Give the preparation type.
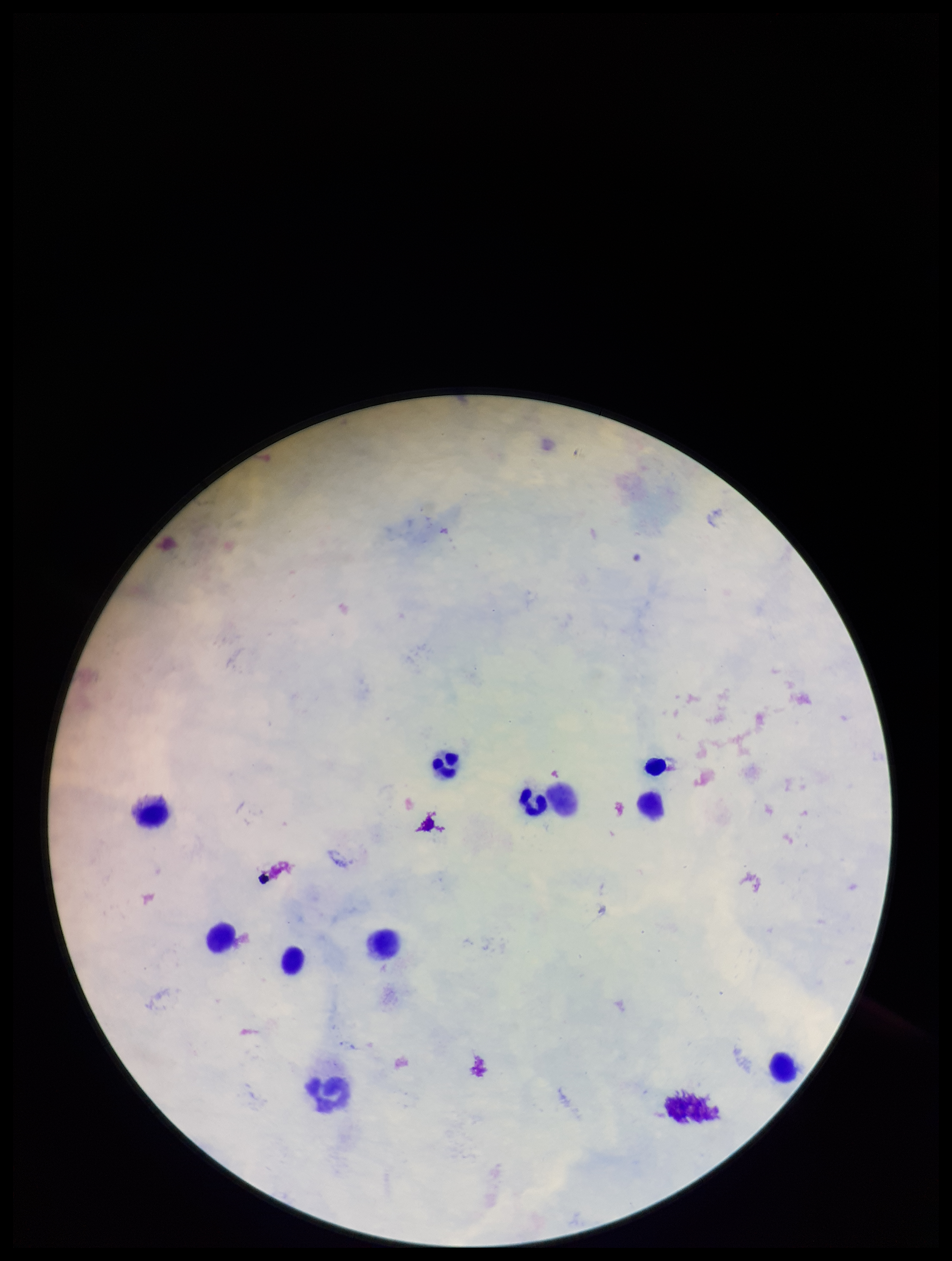
It is a thick blood smear.

Smartphone photograph taken through the eyepiece of a microscope. Patient malaria status: negative. Image is 952×1261 pixels. Parasite count: 0. Leukocyte count: 10. One field from this slide. Plasmodium parasites: none seen. Stained with Giemsa.